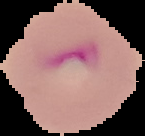
Summary:
  - Image size: 145×136 pixels
  - Malaria status: parasitized
  - Preparation: thin blood film
  - Image type: cell region segmented out of the field of view; surrounding area masked to black